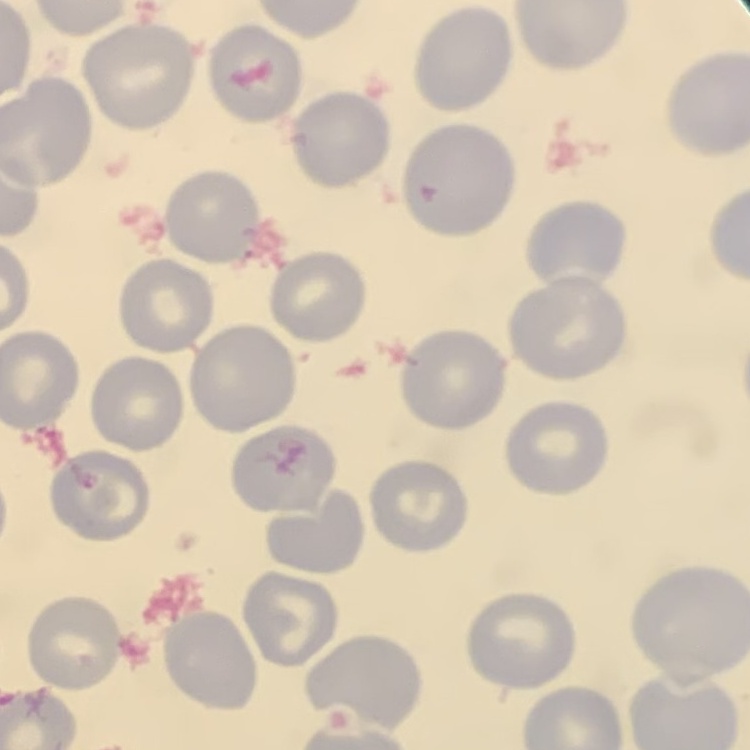
erythrocyte morphology = no rouleaux formation
preparation = thin blood smear
image type = one tile cut from a larger photomicrograph
stain = Field's or Giemsa